Locate every blood parasite and identify its species.
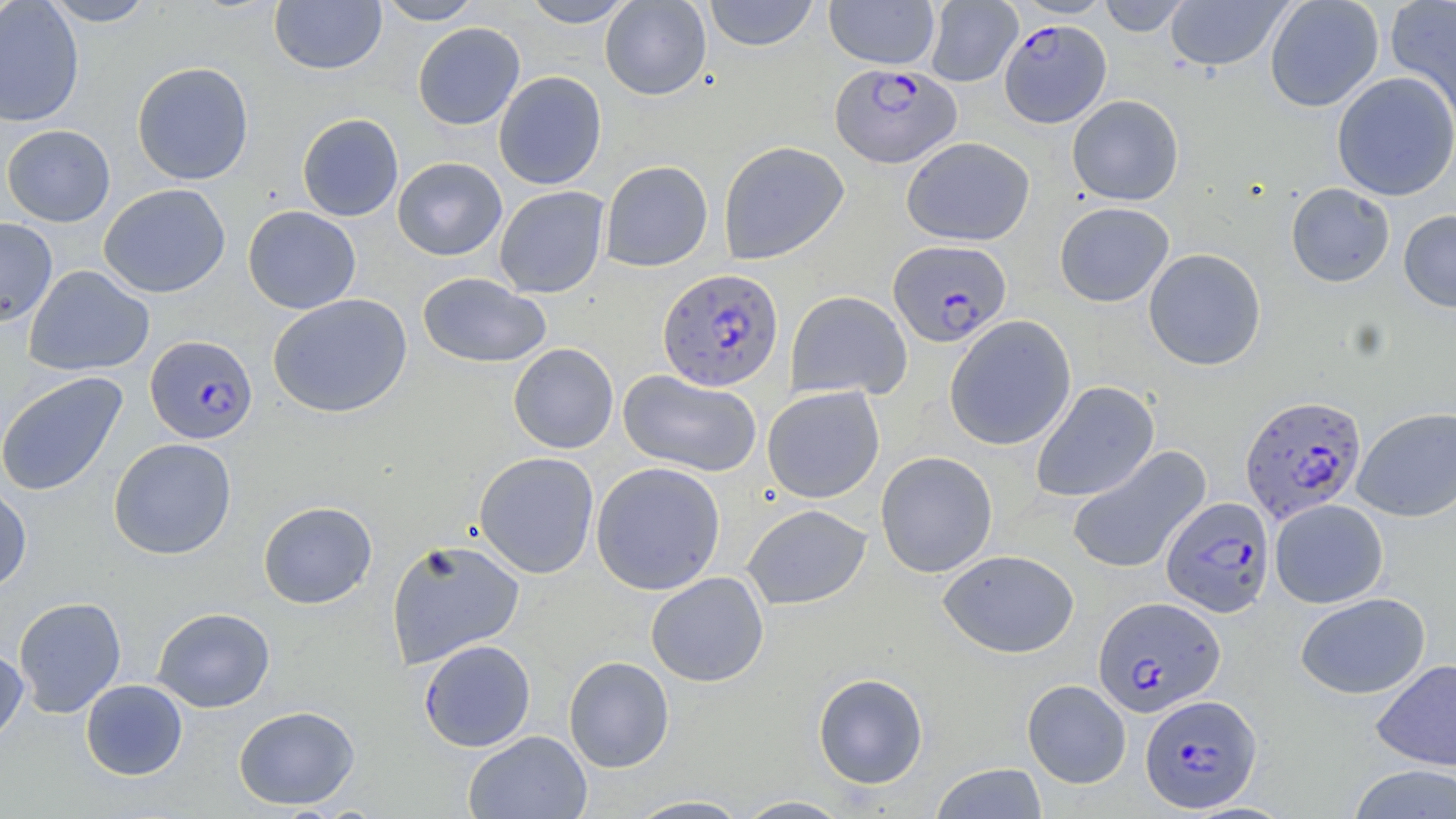
Approximate bounding boxes as (x1,y1)-(x2,y2) corner pairs in pixels.
Plasmodium falciparum-infected red blood cells: (999,20)-(1111,128), (830,63)-(961,168), (888,239)-(1012,347), (658,268)-(785,392), (145,335)-(258,443), (1240,395)-(1367,522), (1161,496)-(1275,617), (1094,595)-(1225,716), (1141,695)-(1261,812).
No Plasmodium ovale, Plasmodium malariae, Plasmodium vivax, Babesia divergens, or Trypanosoma brucei observed.

Uninfected red blood cell locations: (0,0)-(85,128), (41,0)-(156,26), (269,0)-(387,74), (377,0)-(484,25), (522,0)-(636,28), (600,0)-(711,100), (703,0)-(819,51), (824,0)-(940,69), (924,0)-(1021,87), (1012,0)-(1115,18), (1097,0)-(1193,36), (1264,0)-(1384,112), (1385,0)-(1456,124), (1165,1)-(1291,71), (413,22)-(525,130), (131,61)-(254,185), (493,71)-(607,189), (1332,71)-(1456,201), (1067,94)-(1184,205), (297,113)-(404,222), (1,124)-(115,227), (902,136)-(1034,246), (718,140)-(849,264), (392,157)-(507,260), (600,160)-(713,271), (1286,182)-(1395,287), (98,184)-(231,299), (494,186)-(609,298), (1054,202)-(1174,307), (243,206)-(361,314), (1398,210)-(1456,313), (0,217)-(58,326), (1143,248)-(1267,370), (24,265)-(155,377), (417,272)-(551,368), (785,290)-(912,400), (268,293)-(412,417), (944,315)-(1076,450), (508,343)-(619,453), (618,369)-(762,477), (0,371)-(128,497), (1031,381)-(1159,503), (762,386)-(885,503), (1352,407)-(1456,522), (108,438)-(237,560), (1066,446)-(1211,575), (875,451)-(998,578), (474,452)-(599,578), (590,461)-(726,596), (0,481)-(32,595), (1270,499)-(1388,608), (258,501)-(377,609), (742,503)-(871,609), (385,538)-(525,668), (939,549)-(1079,658), (646,572)-(769,687), (1295,593)-(1430,699), (13,596)-(126,718), (152,607)-(276,712), (419,639)-(536,752), (0,644)-(28,747), (563,656)-(674,772), (1371,659)-(1456,771), (813,672)-(928,789), (80,679)-(188,780), (1022,679)-(1131,788), (234,705)-(360,810), (463,730)-(592,819), (930,762)-(1048,819), (1347,764)-(1456,818), (623,795)-(753,818), (733,795)-(854,818). Slide-level diagnosis: Plasmodium falciparum. Light microscopy. Captured at 1000x magnification. One field of a larger specimen. May-Grünwald-Giemsa-stained preparation. Image is 1456×819 pixels. Thin blood film.